Assess for malaria.
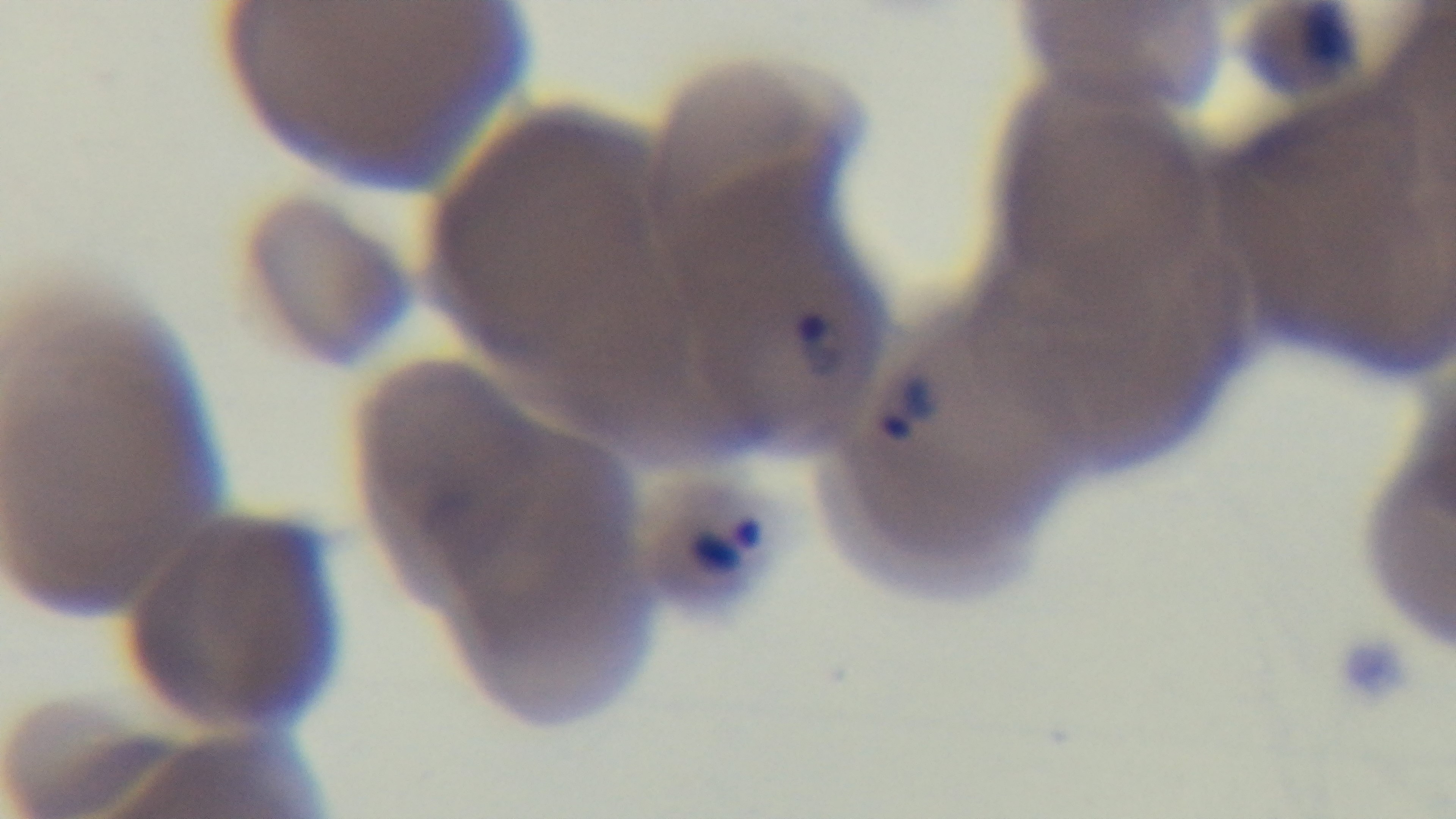
Infected.

Captured with a mounted 4K digital camera. 100x oil-immersion objective. One field from the slide. Preparation: thin blood film. Giemsa-stained. Light microscopy.